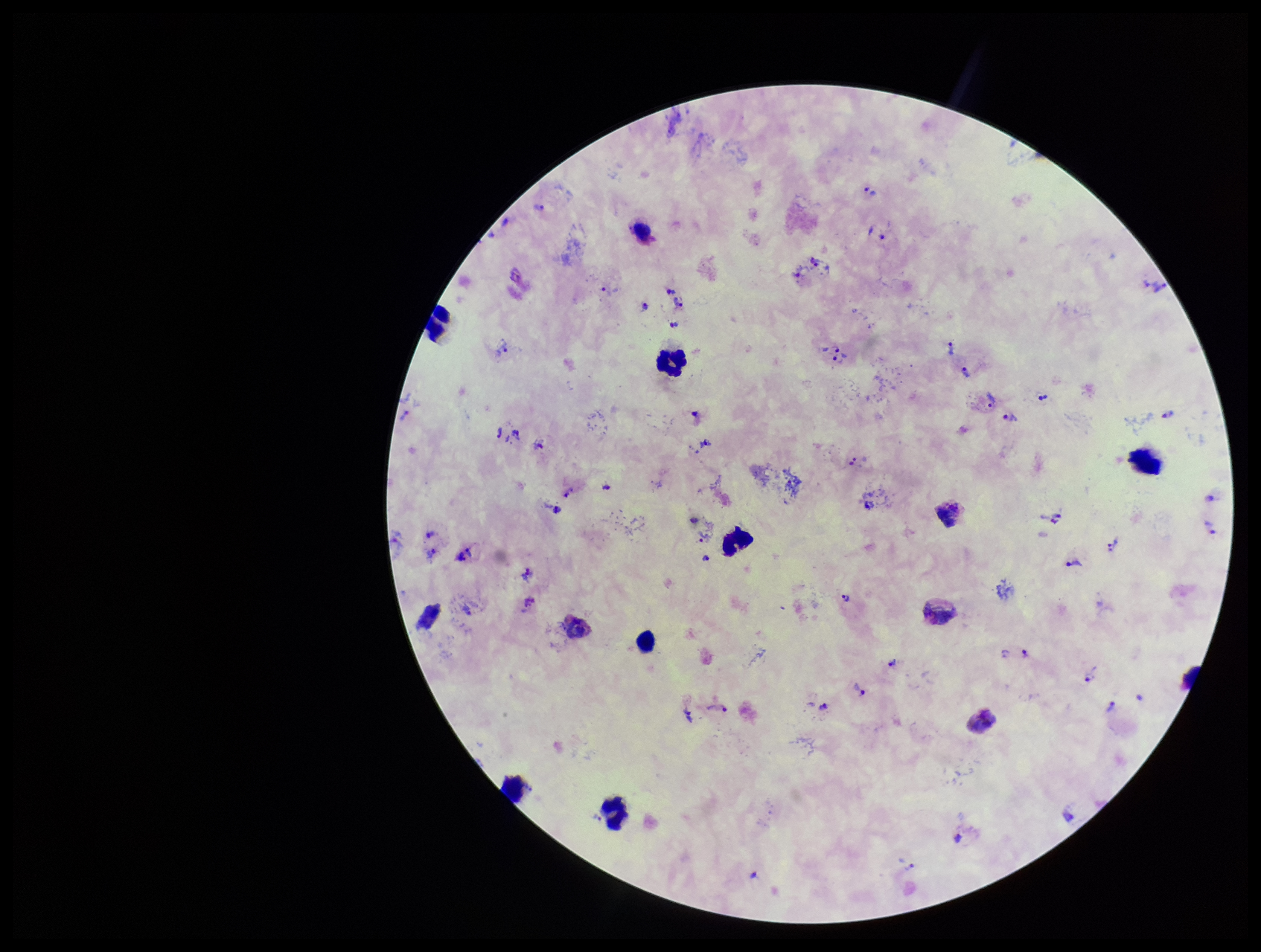
Summary:
  - Leukocyte count: 13
  - Species reported for this patient: Plasmodium vivax
  - Capture: smartphone photograph through the microscope eyepiece
  - Parasite count: 40
  - Image size: 1261×952 pixels
  - Preparation: thick
  - Patient malaria status: infected
  - Stain: Giemsa
  - Field of view: one from this slide
  - Plasmodium parasites: detected